Locate leukocytes (white blood cells).
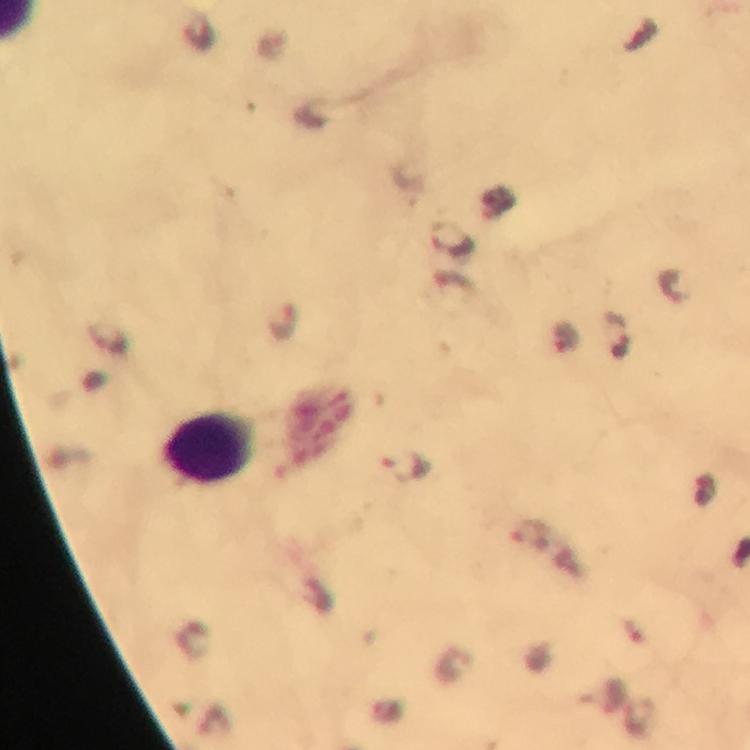
Approximate object centers, in pixels from the top-left corner.
Leukocytes: (x=211, y=448).

Malaria parasite locations: (x=450, y=238), (x=672, y=284), (x=286, y=322), (x=565, y=336), (x=405, y=466), (x=530, y=533). Image is 750×750 pixels. At 100x magnification. Thick blood film. Giemsa stain. From a malaria diagnostic workup. Cropped region of a single field of view. Immersion oil applied. Smartphone photograph taken through a microscope.